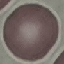
Malaria status: uninfected. Thin smear of blood. Photographed with a smartphone camera at the microscope eyepiece. Cell patch, automatically extracted from a larger field of view and resized to 64 × 64 pixels. Giemsa-stained preparation.